Point out each Plasmodium parasite.
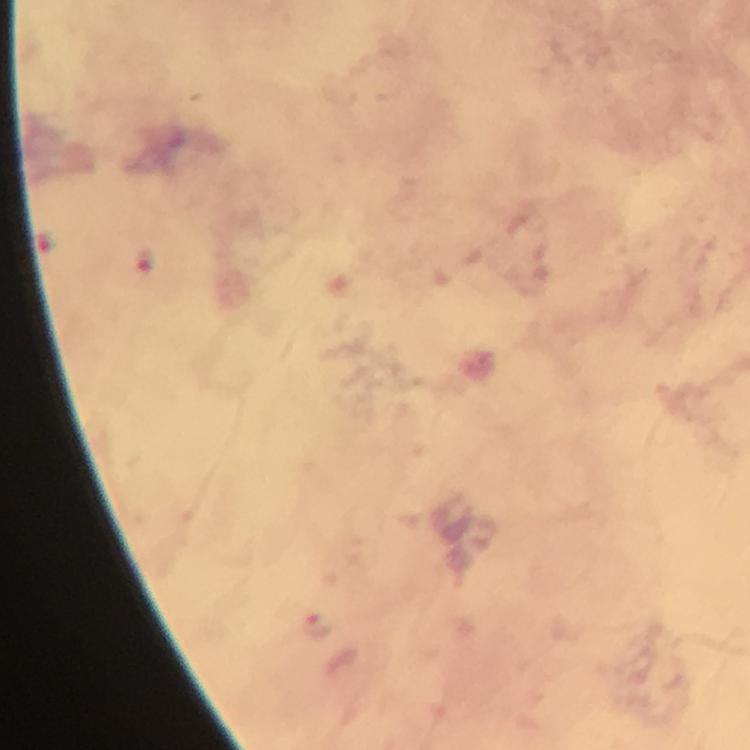
Approximate centers as {x, y} in pixels.
Plasmodium parasites: {146, 258}, {316, 624}.

Summary:
  - Capture: smartphone mounted on the microscope
  - Magnification: 100x
  - Immersion oil: used
  - Context: from a diagnostic examination for malaria
  - Preparation: thick blood smear
  - Cropped from: a single field of view
  - Image size: 750×750 pixels
  - Stain: Giemsa